Report the malaria status of this cell.
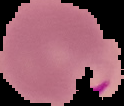
It is parasitized.

Summary:
  - Preparation: thin blood smear
  - Image size: 124×106 pixels
  - Image type: segmented cell region on a black background